Assess this cell for malaria.
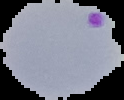

Parasitized.

Segmented cell region on a black background. From a thin blood smear. Image is 124×100 pixels.